State which parasite is depicted.
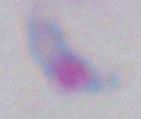

Toxoplasma gondii.

Photomicrograph. Captured at 1000x magnification.